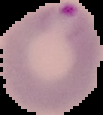
Summary:
  - Image type: cell region segmented out of the field of view; surrounding area masked to black
  - Image size: 103×115 pixels
  - Preparation: thin blood film
  - Malaria status: parasitized